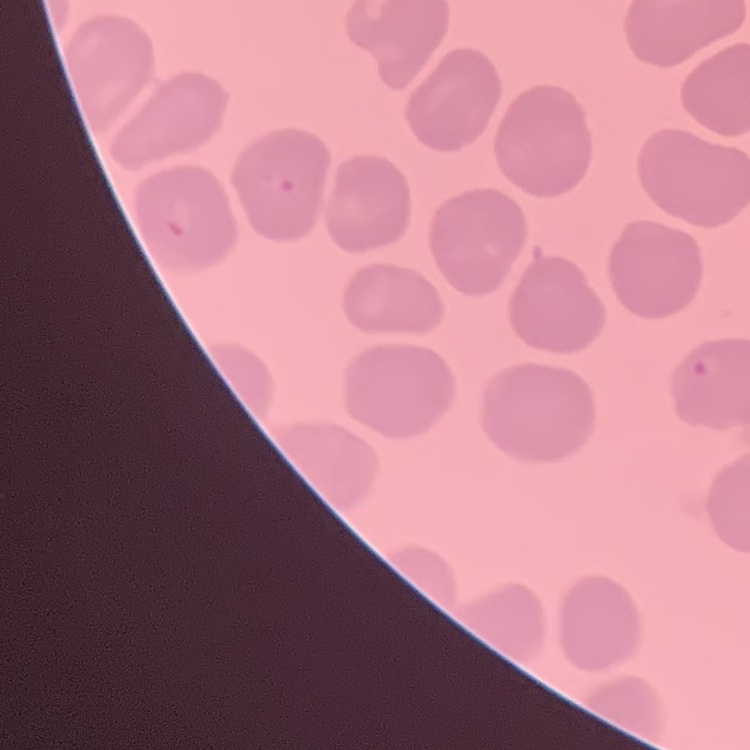 The red blood cells exhibit no rouleaux formation. Square crop of a larger photomicrograph. Stained with either Field's or Giemsa. Thin blood smear.